Point out each leukocyte.
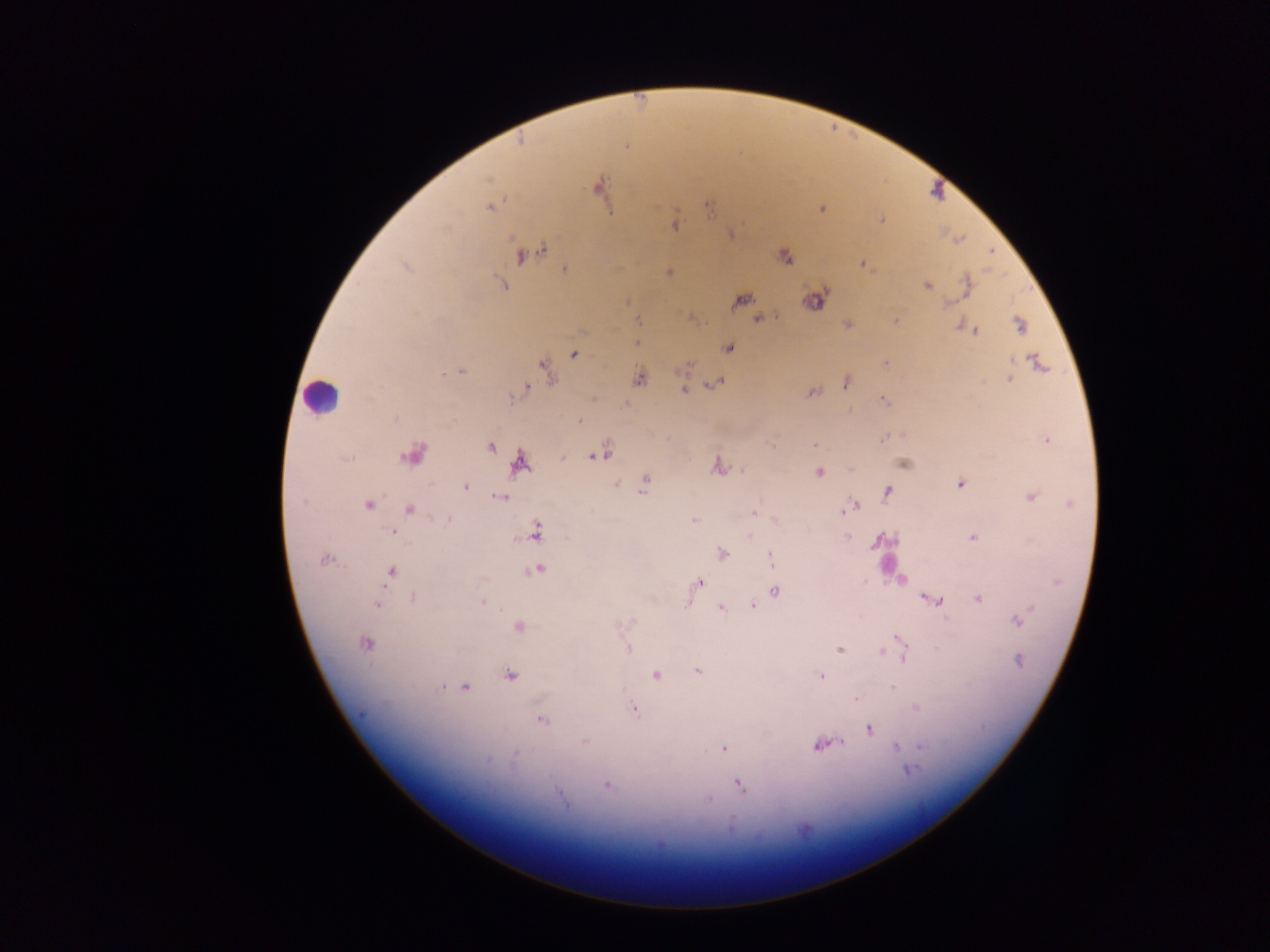

Approximate centers as (x, y) in pixels.
Leukocytes: (322, 396).

Malaria parasite locations: (520, 141), (599, 188), (707, 206), (490, 207), (823, 208), (882, 220), (675, 226), (541, 250), (991, 251), (526, 254), (786, 257), (862, 264), (406, 268), (565, 270), (669, 271), (503, 285), (927, 286), (740, 300), (816, 301), (949, 303), (753, 316), (760, 319), (896, 320), (638, 321), (848, 324), (1021, 326), (974, 331), (637, 343), (729, 349), (574, 355), (885, 363), (1039, 363), (545, 368), (460, 372), (640, 379), (1009, 379), (717, 383), (847, 383), (525, 390), (684, 390), (812, 392), (884, 400), (579, 421), (883, 438), (1047, 441), (814, 445), (491, 446), (413, 455), (595, 456), (345, 460), (519, 463), (905, 463), (718, 465), (819, 473), (645, 482), (616, 484), (960, 484), (465, 487), (643, 491), (887, 491), (1031, 497), (500, 498), (302, 501), (854, 504), (1070, 504), (367, 505), (848, 508), (411, 509), (843, 512), (753, 513), (446, 519), (694, 521), (775, 521), (537, 531), (393, 532), (750, 537), (846, 537), (972, 538), (722, 554), (771, 558), (325, 560), (537, 570), (391, 573), (900, 579), (699, 583), (776, 592), (413, 598), (926, 598), (979, 599), (935, 600), (482, 602), (376, 604), (687, 604), (753, 606), (722, 608), (1017, 620), (518, 627), (900, 639), (366, 644), (628, 648), (901, 649), (839, 650), (883, 652), (904, 657), (1019, 660), (698, 671), (655, 675), (510, 676), (820, 676), (441, 687), (464, 687), (857, 699), (916, 708), (634, 709), (541, 720), (870, 730), (585, 742), (820, 746), (896, 746), (922, 747), (723, 748), (514, 756), (487, 761), (909, 771), (607, 785), (739, 785), (559, 794), (707, 800). Thick blood smear. Single field of view. Collected in Ghana. Photographed through a microscope with a mobile-phone camera. Image is 1270×952 pixels.